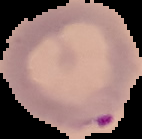

{
  "result": "malaria parasites identified",
  "preparation": "thin blood smear",
  "image_size": "142×139 pixels",
  "image_type": "cell region segmented out of the field of view; surrounding area masked to black"
}